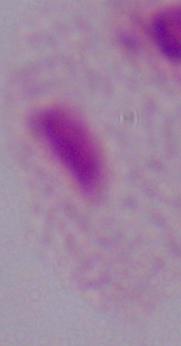
identification: trichomonad
magnification: 1000x
modality: micrograph